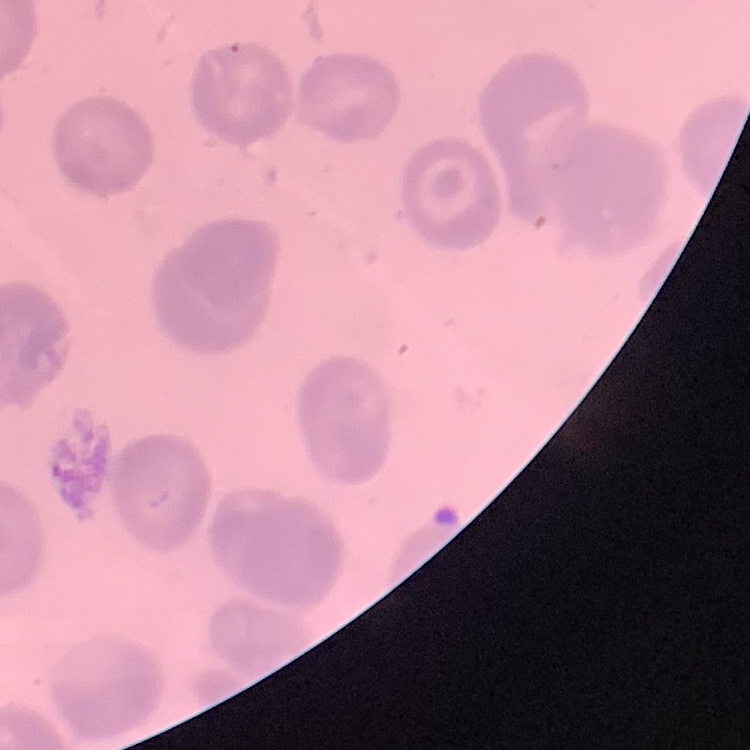

{
  "erythrocyte_morphology": "no rouleaux formation",
  "preparation": "thin blood film",
  "image_type": "square crop of a larger photomicrograph",
  "stain": "Field's or Giemsa"
}